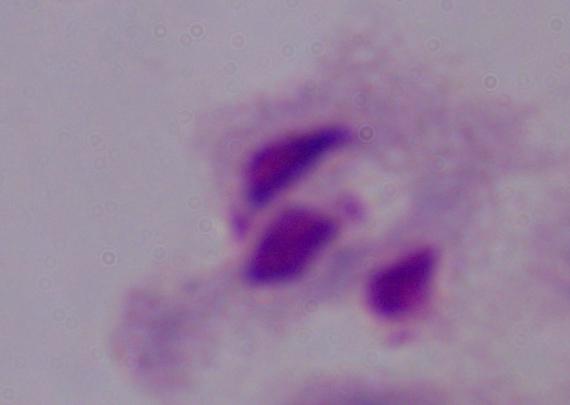
identification = trichomonad
magnification = 1000x
modality = photomicrograph